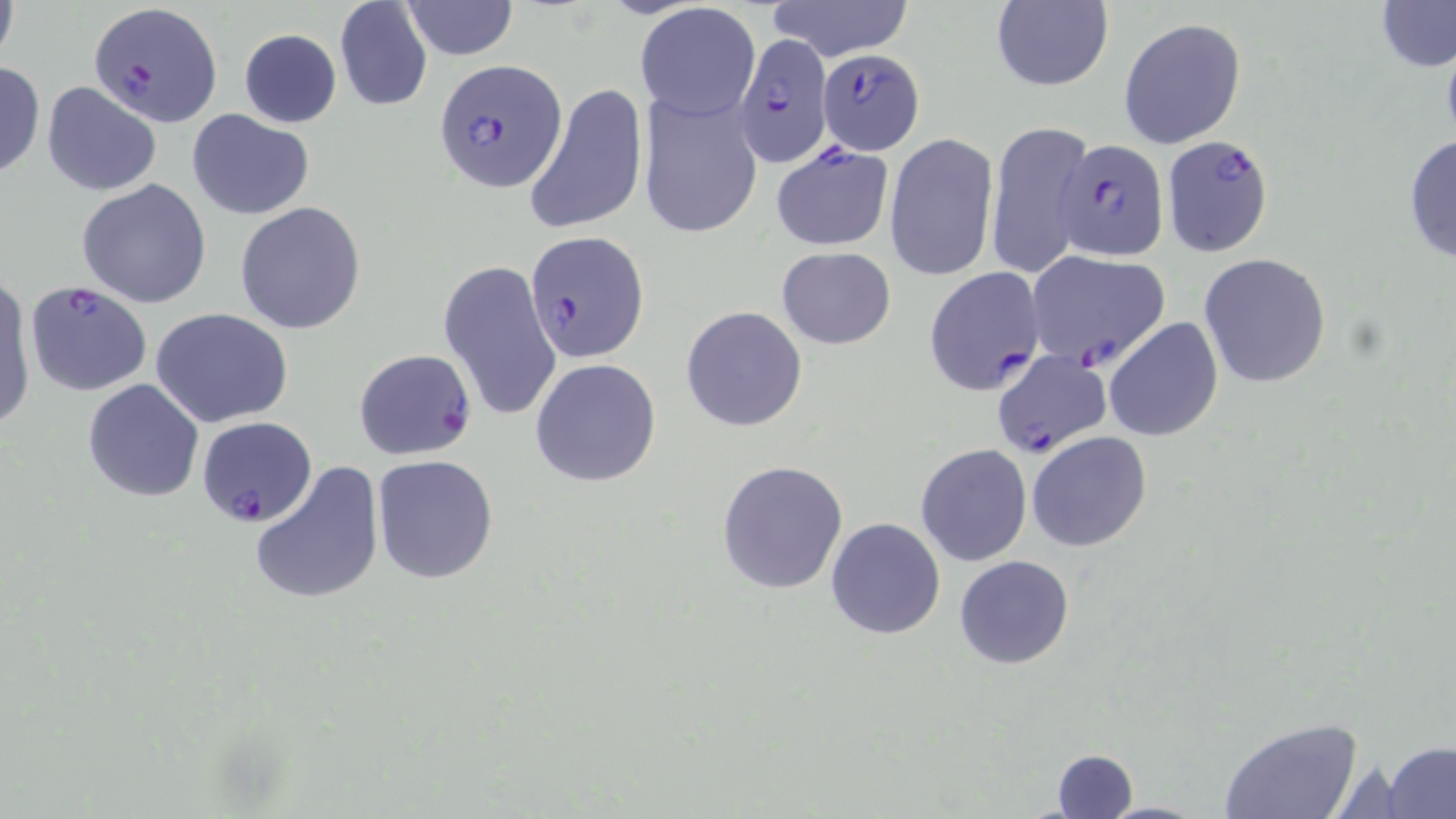

Summary:
  - Coordinate format: approximate bounding boxes as named x1/y1/x2/y2 corners in pixels
  - Plasmodium falciparum-infected red blood cell locations: (x1=89, y1=1, x2=220, y2=127), (x1=735, y1=35, x2=833, y2=168), (x1=817, y1=51, x2=925, y2=153), (x1=434, y1=62, x2=567, y2=194), (x1=1160, y1=135, x2=1272, y2=255), (x1=1055, y1=139, x2=1166, y2=264), (x1=770, y1=142, x2=895, y2=251), (x1=526, y1=230, x2=649, y2=361), (x1=1026, y1=250, x2=1171, y2=370), (x1=922, y1=266, x2=1045, y2=396), (x1=25, y1=280, x2=153, y2=397), (x1=353, y1=349, x2=477, y2=460), (x1=990, y1=349, x2=1111, y2=460), (x1=196, y1=416, x2=317, y2=528)
  - Uninfected red blood cell locations: (x1=0, y1=0, x2=20, y2=69), (x1=332, y1=0, x2=433, y2=113), (x1=767, y1=0, x2=914, y2=61), (x1=1377, y1=0, x2=1455, y2=72), (x1=400, y1=1, x2=519, y2=59), (x1=988, y1=1, x2=1115, y2=93), (x1=635, y1=4, x2=761, y2=121), (x1=1119, y1=17, x2=1246, y2=148), (x1=238, y1=30, x2=342, y2=128), (x1=0, y1=62, x2=45, y2=181), (x1=42, y1=81, x2=162, y2=197), (x1=522, y1=83, x2=647, y2=235), (x1=637, y1=87, x2=763, y2=239), (x1=186, y1=109, x2=315, y2=220), (x1=986, y1=119, x2=1093, y2=280), (x1=885, y1=132, x2=999, y2=281), (x1=1403, y1=133, x2=1456, y2=267), (x1=76, y1=180, x2=212, y2=308), (x1=235, y1=202, x2=367, y2=335), (x1=776, y1=247, x2=897, y2=349), (x1=1197, y1=254, x2=1332, y2=389), (x1=437, y1=258, x2=563, y2=423), (x1=0, y1=274, x2=34, y2=434), (x1=680, y1=308, x2=807, y2=431), (x1=152, y1=309, x2=294, y2=427), (x1=1103, y1=317, x2=1222, y2=442), (x1=529, y1=358, x2=661, y2=487), (x1=82, y1=378, x2=204, y2=503), (x1=1026, y1=431, x2=1152, y2=552), (x1=916, y1=444, x2=1033, y2=566), (x1=373, y1=454, x2=499, y2=583), (x1=717, y1=459, x2=849, y2=595), (x1=249, y1=460, x2=385, y2=606), (x1=825, y1=518, x2=945, y2=639), (x1=954, y1=555, x2=1074, y2=669), (x1=1219, y1=718, x2=1364, y2=819), (x1=1382, y1=740, x2=1455, y2=818), (x1=1050, y1=748, x2=1136, y2=817), (x1=1096, y1=800, x2=1215, y2=818)
  - Slide-level diagnosis: Plasmodium falciparum
  - Magnification: 1000x
  - Preparation: thin blood film
  - Modality: optical microscopy
  - Field of view: single
  - Stain: May-Grünwald-Giemsa
  - Image size: 1456×819 pixels